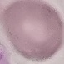

{
  "malaria_status": "uninfected",
  "preparation": "thin blood smear",
  "image_type": "automatically extracted cell patch, resized to 64 × 64 pixels",
  "stain": "Giemsa",
  "capture": "smartphone camera at the microscope eyepiece"
}